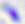

Photomicrograph. Toxoplasma gondii is seen. Captured at 400x magnification.